State which cell type is depicted.
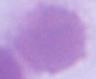

An erythrocyte.

1000x magnification. Photomicrograph.